Give the position of every Plasmodium parasite.
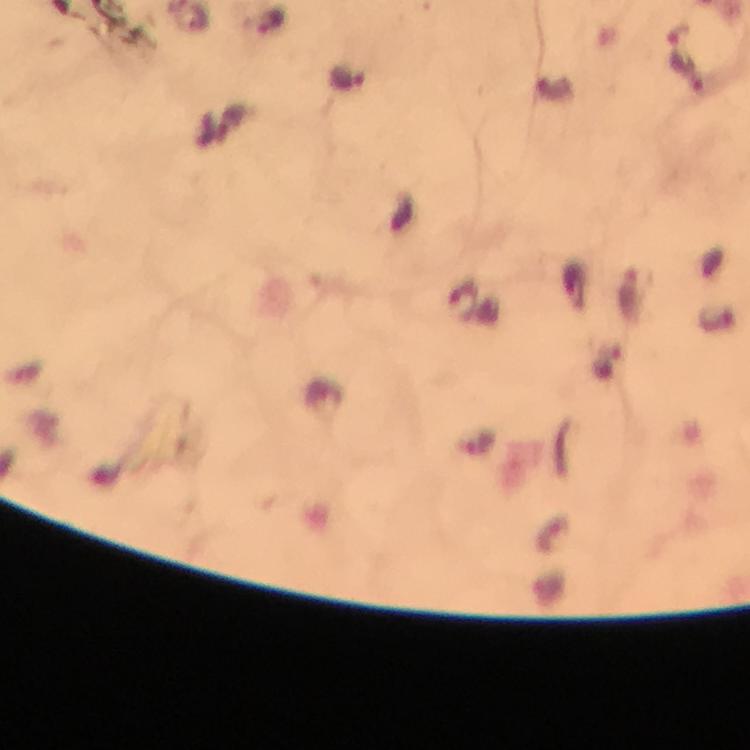
Approximate object centers, in pixels from the top-left corner.
Plasmodium parasites: (x=687, y=73), (x=347, y=77), (x=462, y=303).

Thick blood smear. Image is 750×750 pixels. Smartphone photograph taken through a microscope. Immersion oil applied. From a diagnostic examination for malaria. 100x magnification. Giemsa stain. Cropped region of a single field of view.